Outline each blood parasite and name the species.
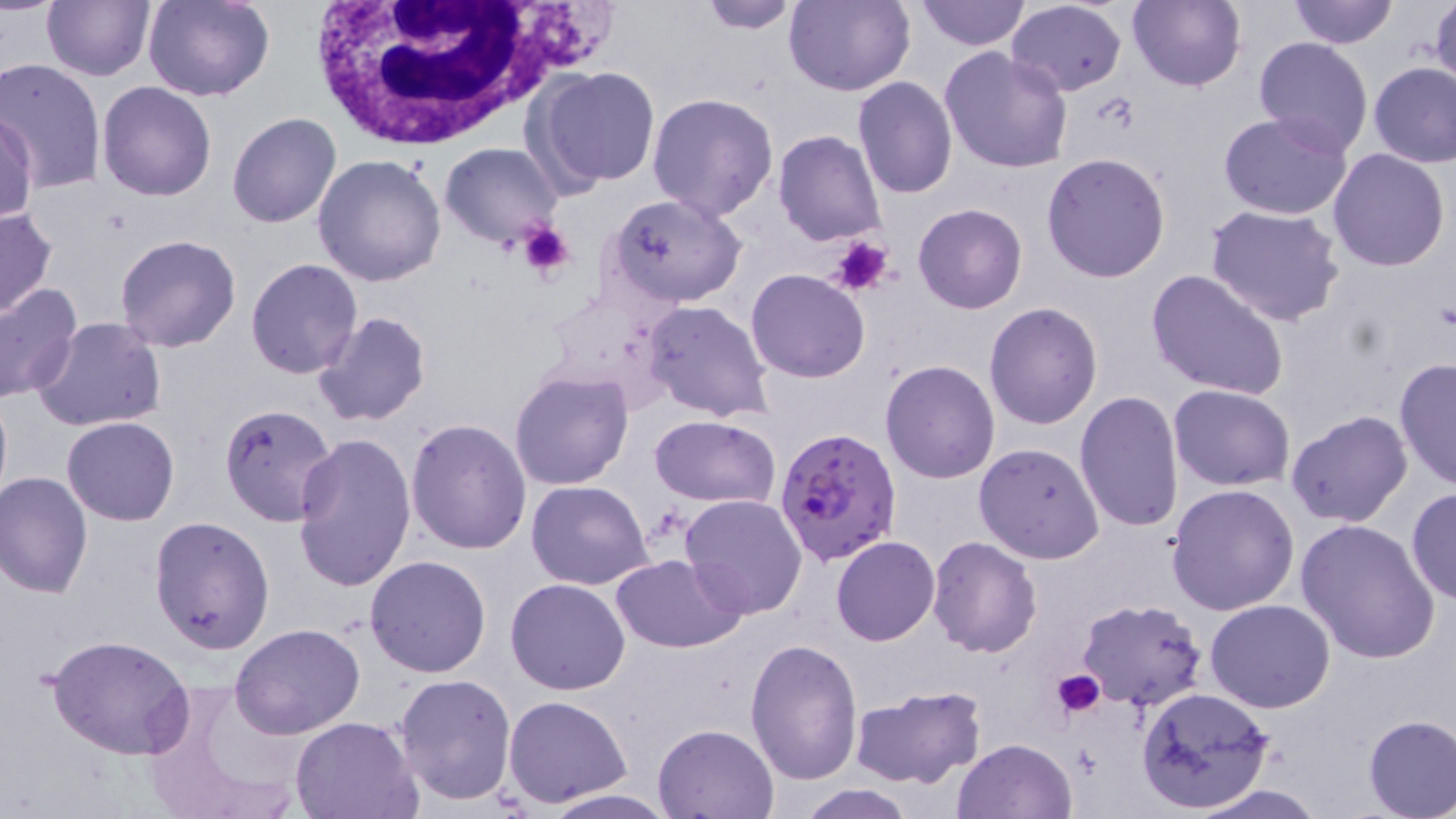
Approximate bounding boxes as named x1/y1/x2/y2 corners in pixels.
Plasmodium falciparum-infected red blood cells: (x1=775, y1=426, x2=903, y2=566).
No Plasmodium ovale, Plasmodium malariae, Plasmodium vivax, Babesia divergens, or Trypanosoma brucei observed.

Summary:
  - Platelet locations: (x1=516, y1=221, x2=576, y2=283), (x1=829, y1=235, x2=892, y2=297), (x1=1052, y1=669, x2=1105, y2=719)
  - White blood cell locations: (x1=301, y1=0, x2=563, y2=151)
  - Uninfected red blood cell locations: (x1=41, y1=0, x2=155, y2=81), (x1=142, y1=0, x2=276, y2=102), (x1=692, y1=0, x2=807, y2=33), (x1=784, y1=0, x2=913, y2=97), (x1=915, y1=0, x2=1031, y2=51), (x1=1125, y1=0, x2=1246, y2=91), (x1=1289, y1=0, x2=1398, y2=47), (x1=1428, y1=0, x2=1456, y2=94), (x1=1005, y1=1, x2=1128, y2=95), (x1=1253, y1=37, x2=1373, y2=157), (x1=939, y1=47, x2=1073, y2=174), (x1=0, y1=58, x2=106, y2=195), (x1=1369, y1=62, x2=1456, y2=167), (x1=533, y1=66, x2=660, y2=191), (x1=853, y1=77, x2=957, y2=200), (x1=97, y1=82, x2=217, y2=201), (x1=646, y1=92, x2=778, y2=223), (x1=1, y1=109, x2=39, y2=225), (x1=227, y1=112, x2=342, y2=228), (x1=1218, y1=112, x2=1353, y2=221), (x1=773, y1=129, x2=886, y2=246), (x1=440, y1=142, x2=563, y2=248), (x1=1328, y1=149, x2=1450, y2=272), (x1=1042, y1=152, x2=1170, y2=283), (x1=312, y1=153, x2=447, y2=286), (x1=607, y1=194, x2=749, y2=306), (x1=913, y1=203, x2=1028, y2=314), (x1=1205, y1=203, x2=1346, y2=326), (x1=0, y1=205, x2=58, y2=321), (x1=113, y1=235, x2=241, y2=354), (x1=245, y1=258, x2=363, y2=379), (x1=1145, y1=268, x2=1290, y2=401), (x1=745, y1=269, x2=872, y2=383), (x1=0, y1=281, x2=82, y2=402), (x1=641, y1=300, x2=775, y2=423), (x1=984, y1=302, x2=1103, y2=430), (x1=312, y1=311, x2=433, y2=427), (x1=32, y1=317, x2=169, y2=433), (x1=1395, y1=358, x2=1456, y2=489), (x1=880, y1=360, x2=1001, y2=483), (x1=509, y1=370, x2=635, y2=491), (x1=0, y1=384, x2=11, y2=511), (x1=1168, y1=384, x2=1294, y2=491), (x1=1074, y1=391, x2=1185, y2=534), (x1=219, y1=403, x2=340, y2=528), (x1=1287, y1=411, x2=1413, y2=528), (x1=648, y1=414, x2=780, y2=508), (x1=63, y1=415, x2=180, y2=526), (x1=405, y1=418, x2=532, y2=556), (x1=291, y1=432, x2=416, y2=594), (x1=974, y1=442, x2=1105, y2=564), (x1=0, y1=470, x2=93, y2=598), (x1=525, y1=479, x2=653, y2=589), (x1=1166, y1=484, x2=1300, y2=615), (x1=1407, y1=487, x2=1456, y2=606), (x1=681, y1=494, x2=807, y2=618), (x1=149, y1=514, x2=276, y2=656), (x1=1296, y1=518, x2=1441, y2=664), (x1=832, y1=535, x2=941, y2=646), (x1=927, y1=535, x2=1041, y2=656), (x1=365, y1=555, x2=492, y2=677), (x1=611, y1=555, x2=747, y2=653), (x1=505, y1=577, x2=632, y2=694), (x1=1076, y1=599, x2=1206, y2=710), (x1=1205, y1=601, x2=1334, y2=714), (x1=231, y1=623, x2=366, y2=738), (x1=48, y1=635, x2=195, y2=759), (x1=746, y1=635, x2=864, y2=783), (x1=394, y1=673, x2=517, y2=805), (x1=141, y1=678, x2=307, y2=819), (x1=849, y1=684, x2=988, y2=789), (x1=1135, y1=688, x2=1275, y2=814), (x1=503, y1=695, x2=632, y2=806), (x1=1361, y1=714, x2=1456, y2=818), (x1=288, y1=715, x2=421, y2=819), (x1=653, y1=722, x2=778, y2=817), (x1=952, y1=738, x2=1077, y2=819), (x1=796, y1=783, x2=916, y2=818), (x1=1180, y1=784, x2=1329, y2=819), (x1=540, y1=788, x2=678, y2=818)
  - Slide-level diagnosis: Plasmodium falciparum
  - Modality: optical microscopy
  - Stain: May-Grünwald-Giemsa
  - Magnification: 1000x
  - Image size: 1456×819 pixels
  - Field of view: single
  - Preparation: thin blood smear